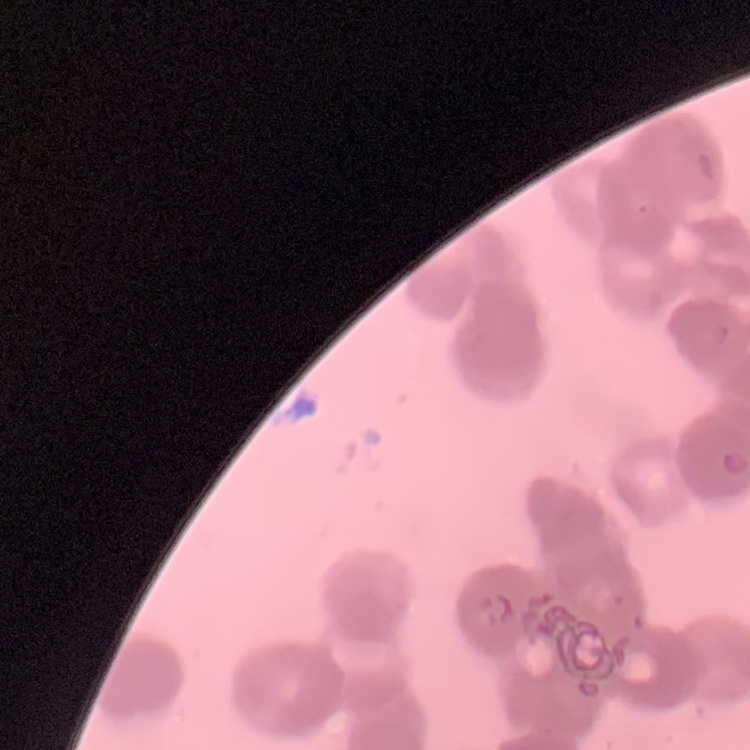 The red blood cells exhibit rouleaux formation. Thin blood smear. One tile cut from a larger photomicrograph. Field's or Giemsa stain.